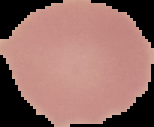

Summary:
  - Malaria status: uninfected
  - Image size: 154×127 pixels
  - Preparation: thin blood film
  - Image type: segmented cell region with the area outside set to black